Identify the preparation type.
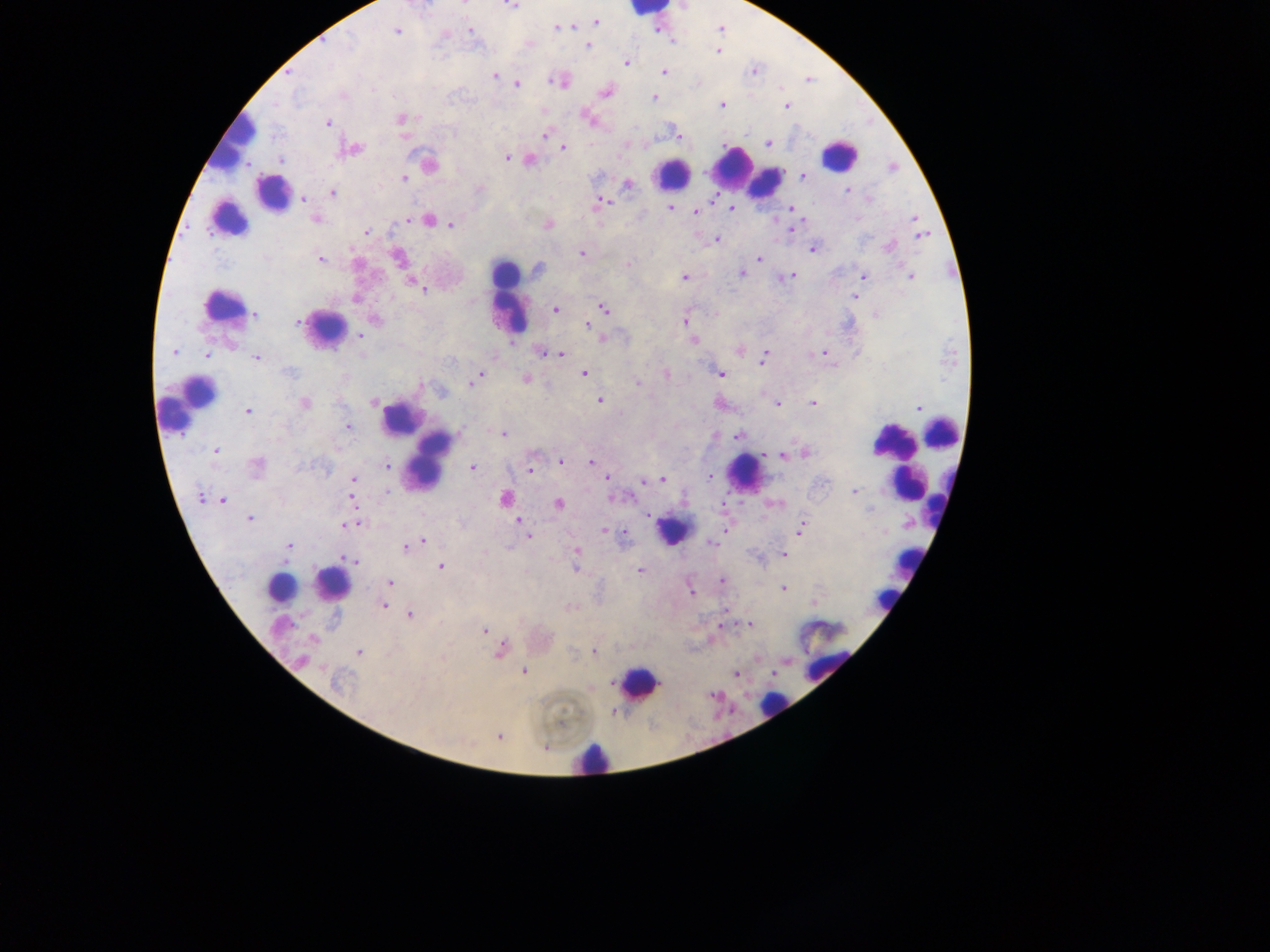
This is a thick smear.

leukocyte locations = approximate centers as {x, y} in pixels: {650, 11}, {233, 138}, {838, 155}, {735, 167}, {673, 173}, {764, 181}, {273, 192}, {227, 220}, {506, 274}, {509, 297}, {220, 304}, {326, 327}, {192, 401}, {401, 419}, {941, 432}, {415, 439}, {891, 440}, {429, 459}, {903, 465}, {744, 472}, {904, 483}, {672, 529}, {907, 561}, {332, 584}, {306, 585}, {280, 587}, {882, 599}, {826, 674}, {638, 682}, {773, 705}, {590, 757}
country = Ghana
image size = 1270×952 pixels
field of view = single
Plasmodium parasite locations = approximate centers as {x, y} in pixels: {463, 4}, {510, 5}, {596, 22}, {574, 26}, {558, 28}, {471, 30}, {397, 32}, {350, 42}, {588, 46}, {718, 51}, {627, 62}, {753, 71}, {664, 72}, {288, 73}, {494, 76}, {556, 81}, {517, 85}, {606, 91}, {342, 95}, {653, 98}, {722, 105}, {786, 106}, {400, 118}, {588, 118}, {327, 123}, {544, 135}, {679, 135}, {768, 143}, {563, 148}, {352, 149}, {506, 157}, {281, 160}, {530, 160}, {429, 164}, {893, 167}, {803, 176}, {404, 178}, {628, 185}, {847, 190}, {333, 193}, {303, 199}, {601, 202}, {734, 208}, {670, 209}, {696, 212}, {315, 219}, {915, 219}, {409, 220}, {429, 220}, {450, 224}, {549, 224}, {791, 229}, {367, 232}, {922, 235}, {716, 240}, {889, 246}, {813, 249}, {582, 253}, {398, 257}, {759, 258}, {320, 259}, {628, 263}, {537, 270}, {741, 272}, {791, 276}, {863, 276}, {684, 277}, {910, 277}, {415, 284}, {421, 288}, {855, 296}, {356, 299}, {603, 309}, {555, 310}, {254, 315}, {375, 320}, {685, 320}, {297, 322}, {587, 325}, {360, 335}, {693, 340}, {739, 350}, {174, 352}, {543, 352}, {823, 353}, {207, 355}, {561, 355}, {256, 357}, {763, 357}, {288, 372}, {584, 374}, {666, 374}, {720, 374}, {479, 376}, {525, 379}, {472, 382}, {638, 383}, {422, 386}, {600, 401}, {374, 402}, {812, 403}, {304, 404}, {777, 404}, {919, 407}, {248, 411}, {348, 426}, {503, 434}, {738, 435}, {216, 450}, {806, 453}, {781, 455}, {561, 461}, {591, 462}, {256, 465}, {386, 466}, {472, 468}, {530, 469}, {606, 477}, {709, 477}, {353, 479}, {662, 479}, {644, 481}, {388, 492}, {853, 492}, {617, 497}, {200, 498}, {505, 498}, {223, 500}, {353, 500}, {559, 504}, {869, 508}, {647, 515}, {249, 518}, {518, 521}, {356, 523}, {348, 525}, {801, 528}, {606, 532}, {528, 537}, {422, 542}, {416, 543}, {711, 543}, {288, 546}, {407, 547}, {576, 551}, {783, 555}, {350, 560}, {441, 566}, {640, 571}, {722, 580}, {390, 582}, {783, 588}, {384, 606}, {410, 615}, {749, 625}, {484, 631}, {313, 639}, {500, 651}, {595, 651}, {359, 652}, {302, 660}, {524, 671}, {736, 674}, {337, 682}, {714, 696}, {498, 736}, {545, 748}
capture = mobile-phone photograph through a microscope